Assess this cell for malaria.
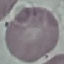

It is uninfected.

Summary:
  - Preparation: thin smear
  - Capture: smartphone through the microscope eyepiece
  - Stain: Giemsa
  - Image type: cell patch, automatically extracted from a larger field of view and resized to 64 × 64 pixels